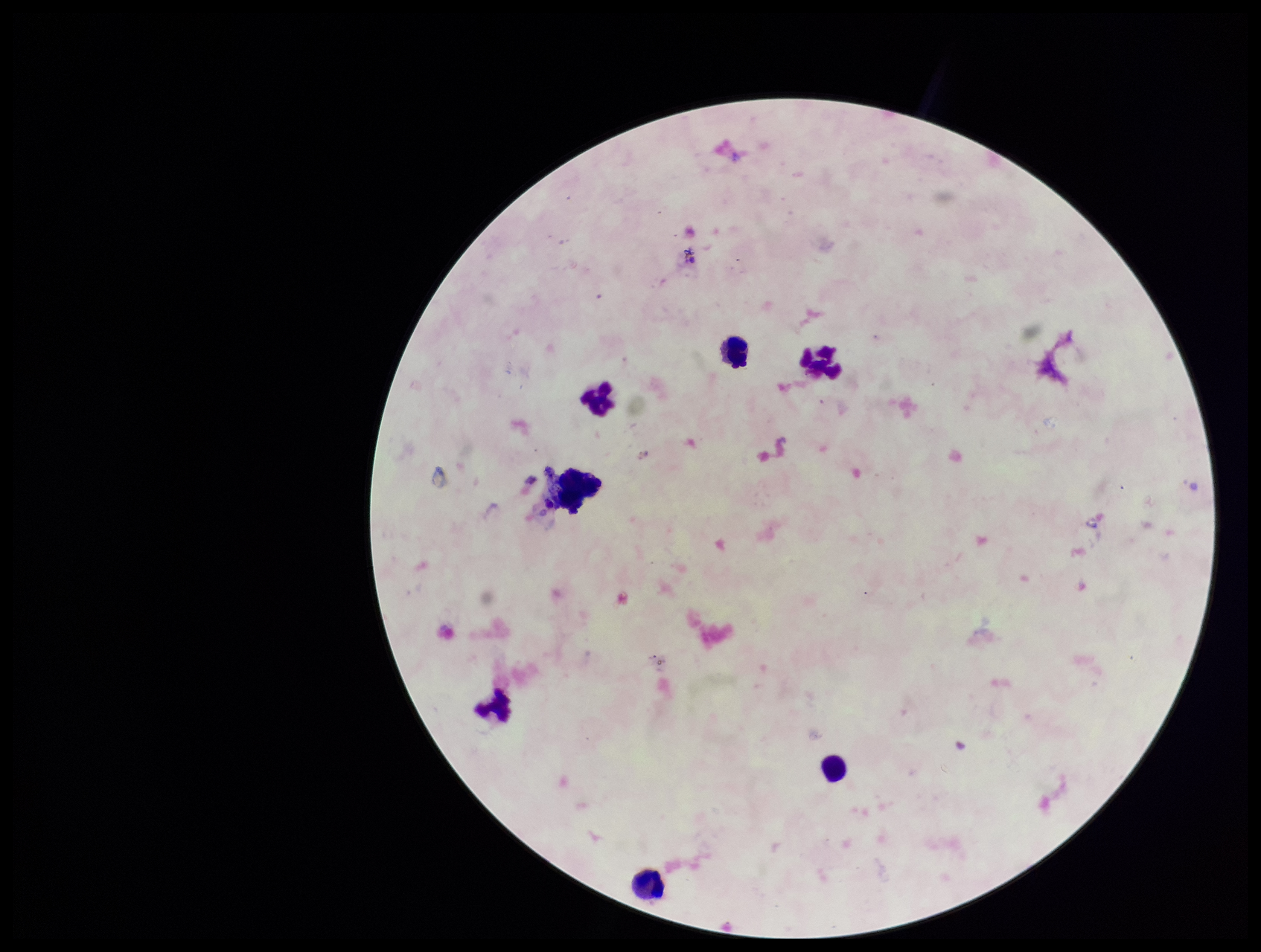 Parasite count: 0. Leukocyte count: 7. Preparation: thick smear. Image is 1261×952 pixels. Smartphone photograph taken through the eyepiece of a microscope. Patient malaria status: negative. One field from this slide. Plasmodium parasites: none identified. Stained with Giemsa.